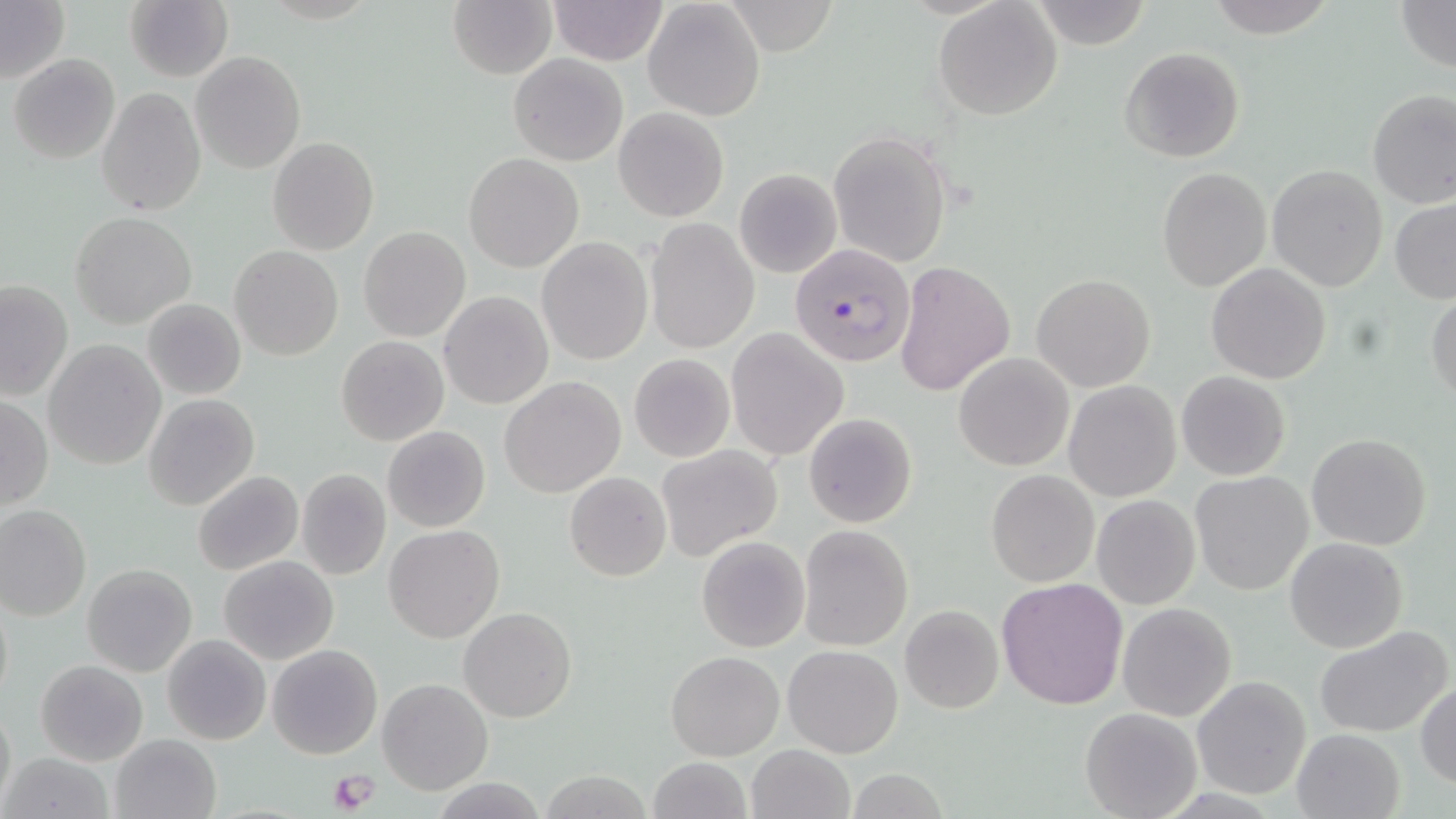 Approximate bounding boxes as [x1, y1, x2, y2] in pixels. Plasmodium falciparum-infected red blood cell locations: [789, 243, 917, 369]. Platelet locations: [327, 768, 380, 815]. Uninfected red blood cell locations: [124, 0, 233, 83], [1027, 0, 1152, 49], [1202, 0, 1336, 36], [1395, 0, 1456, 72], [0, 1, 70, 84], [448, 1, 556, 79], [547, 1, 669, 65], [643, 1, 765, 122], [934, 2, 1062, 121], [1119, 47, 1246, 163], [191, 50, 306, 174], [8, 53, 120, 164], [508, 53, 629, 166], [128, 77, 302, 200], [98, 87, 206, 216], [1367, 89, 1456, 208], [613, 107, 729, 222], [829, 130, 952, 268], [267, 136, 379, 255], [463, 153, 585, 273], [1267, 164, 1388, 291], [1156, 167, 1272, 293], [735, 169, 841, 278], [1389, 197, 1456, 304], [70, 212, 196, 327], [645, 219, 759, 354], [358, 226, 471, 343], [537, 237, 653, 365], [229, 246, 344, 362], [893, 260, 1015, 396], [1207, 263, 1332, 384], [1031, 275, 1157, 393], [0, 280, 73, 401], [1426, 290, 1456, 407], [439, 291, 552, 409], [143, 299, 246, 400], [726, 328, 850, 460], [337, 335, 448, 445], [43, 339, 166, 470], [628, 353, 735, 463], [954, 353, 1075, 472], [1176, 371, 1291, 480], [499, 376, 626, 498], [1064, 380, 1181, 502], [143, 393, 261, 511], [0, 397, 53, 511], [804, 412, 917, 528], [382, 426, 491, 532], [1306, 433, 1433, 549], [656, 445, 784, 563], [295, 468, 391, 580], [986, 469, 1100, 586], [193, 471, 304, 576], [565, 471, 672, 582], [1190, 471, 1314, 595], [1090, 495, 1200, 609], [0, 504, 92, 620], [797, 524, 916, 651], [384, 525, 504, 642], [696, 536, 812, 653], [1284, 537, 1407, 653], [218, 555, 339, 665], [82, 563, 197, 677], [996, 576, 1128, 709], [0, 589, 14, 710], [1117, 602, 1236, 720], [900, 605, 1004, 714], [459, 607, 576, 723], [1315, 624, 1452, 738], [162, 633, 271, 746], [267, 643, 383, 760], [783, 644, 904, 758], [665, 648, 784, 761], [35, 660, 149, 766], [1190, 675, 1311, 801], [377, 677, 493, 795], [1415, 681, 1456, 787], [0, 699, 15, 812], [1080, 707, 1202, 819], [1291, 729, 1404, 818], [110, 733, 222, 818], [746, 744, 855, 819], [3, 752, 115, 819], [646, 757, 753, 818], [843, 769, 949, 819], [536, 772, 657, 817], [430, 777, 549, 817]. Slide-level diagnosis: Plasmodium falciparum. 1000x magnification. One field of a larger specimen. May-Grünwald-Giemsa stain. Thin blood smear. Optical microscopy. Image is 1456×819 pixels.